Classify this cell by malaria status.
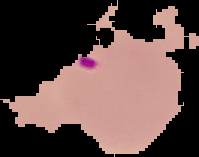
Parasitized.

preparation: thin blood film
image_size: 199×157 pixels
image_type: segmented cell region on a black background